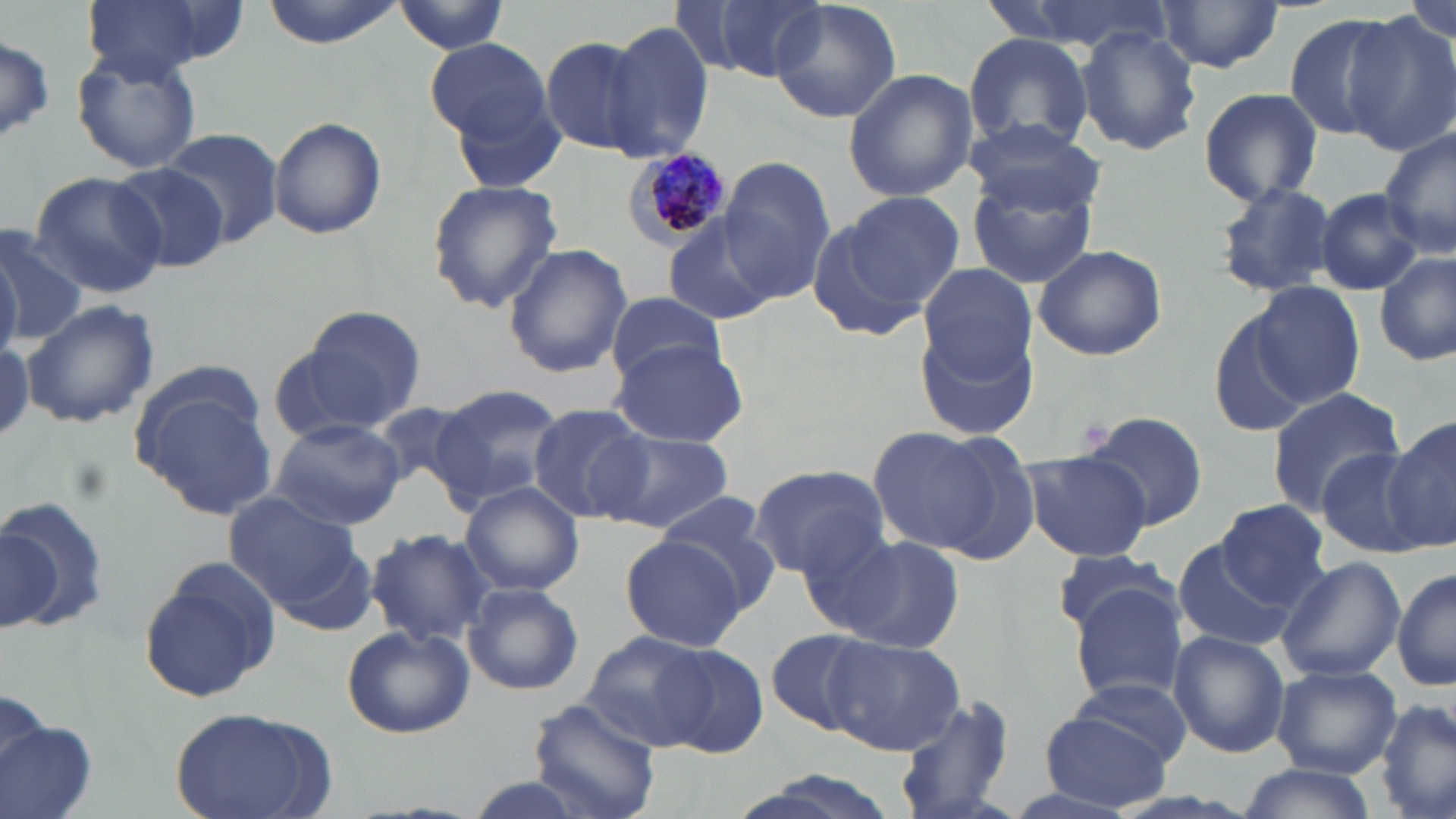

Summary:
  - Coordinate format: approximate bounding boxes as named x1/y1/x2/y2 corners in pixels
  - Plasmodium malariae-infected red blood cell locations: (x1=624, y1=147, x2=733, y2=248)
  - Uninfected red blood cell locations: (x1=76, y1=0, x2=222, y2=83), (x1=261, y1=0, x2=409, y2=49), (x1=394, y1=0, x2=511, y2=53), (x1=688, y1=0, x2=832, y2=82), (x1=768, y1=0, x2=902, y2=123), (x1=1406, y1=0, x2=1454, y2=45), (x1=1155, y1=2, x2=1284, y2=75), (x1=1282, y1=12, x2=1403, y2=141), (x1=1346, y1=12, x2=1456, y2=155), (x1=603, y1=20, x2=716, y2=161), (x1=1074, y1=22, x2=1202, y2=158), (x1=538, y1=33, x2=660, y2=158), (x1=961, y1=34, x2=1094, y2=154), (x1=0, y1=35, x2=55, y2=145), (x1=423, y1=36, x2=552, y2=141), (x1=71, y1=48, x2=202, y2=173), (x1=844, y1=68, x2=978, y2=202), (x1=1198, y1=86, x2=1323, y2=207), (x1=450, y1=91, x2=571, y2=192), (x1=268, y1=116, x2=386, y2=241), (x1=963, y1=118, x2=1103, y2=218), (x1=1378, y1=125, x2=1456, y2=259), (x1=158, y1=127, x2=284, y2=249), (x1=717, y1=157, x2=835, y2=302), (x1=107, y1=162, x2=231, y2=274), (x1=29, y1=171, x2=165, y2=297), (x1=965, y1=173, x2=1097, y2=290), (x1=425, y1=179, x2=563, y2=315), (x1=1211, y1=180, x2=1341, y2=300), (x1=1315, y1=188, x2=1426, y2=294), (x1=843, y1=192, x2=966, y2=311), (x1=663, y1=215, x2=772, y2=326), (x1=803, y1=215, x2=920, y2=342), (x1=0, y1=224, x2=86, y2=347), (x1=1032, y1=242, x2=1168, y2=361), (x1=502, y1=243, x2=632, y2=378), (x1=0, y1=244, x2=20, y2=364), (x1=1376, y1=250, x2=1454, y2=369), (x1=917, y1=262, x2=1037, y2=378), (x1=1249, y1=280, x2=1366, y2=406), (x1=605, y1=289, x2=725, y2=388), (x1=20, y1=300, x2=159, y2=431), (x1=1210, y1=304, x2=1318, y2=439), (x1=289, y1=305, x2=430, y2=434), (x1=916, y1=321, x2=1040, y2=444), (x1=608, y1=338, x2=754, y2=447), (x1=428, y1=384, x2=567, y2=510), (x1=1265, y1=387, x2=1408, y2=517), (x1=136, y1=389, x2=279, y2=520), (x1=528, y1=404, x2=655, y2=523), (x1=1078, y1=409, x2=1207, y2=534), (x1=1379, y1=415, x2=1456, y2=551), (x1=269, y1=418, x2=406, y2=530), (x1=869, y1=428, x2=1008, y2=554), (x1=597, y1=429, x2=734, y2=532), (x1=1318, y1=447, x2=1429, y2=557), (x1=1021, y1=450, x2=1155, y2=562), (x1=746, y1=465, x2=890, y2=577), (x1=460, y1=482, x2=584, y2=597), (x1=223, y1=491, x2=368, y2=622), (x1=657, y1=495, x2=777, y2=597), (x1=0, y1=498, x2=109, y2=637), (x1=1206, y1=502, x2=1331, y2=611), (x1=1, y1=524, x2=63, y2=632), (x1=791, y1=526, x2=911, y2=637), (x1=362, y1=528, x2=493, y2=648), (x1=828, y1=534, x2=964, y2=654), (x1=620, y1=536, x2=746, y2=651), (x1=1171, y1=537, x2=1296, y2=652), (x1=1049, y1=548, x2=1177, y2=635), (x1=1274, y1=556, x2=1405, y2=683), (x1=137, y1=558, x2=281, y2=703), (x1=1392, y1=568, x2=1456, y2=691), (x1=463, y1=583, x2=584, y2=696), (x1=1068, y1=585, x2=1191, y2=705), (x1=341, y1=624, x2=475, y2=740), (x1=581, y1=627, x2=718, y2=751), (x1=765, y1=627, x2=881, y2=738), (x1=1166, y1=629, x2=1289, y2=759), (x1=823, y1=634, x2=966, y2=755), (x1=655, y1=642, x2=768, y2=757), (x1=1271, y1=664, x2=1403, y2=779), (x1=1070, y1=674, x2=1193, y2=772), (x1=0, y1=690, x2=50, y2=786), (x1=893, y1=694, x2=1018, y2=819), (x1=1376, y1=696, x2=1455, y2=819), (x1=528, y1=698, x2=661, y2=819), (x1=167, y1=707, x2=337, y2=819), (x1=1038, y1=709, x2=1174, y2=811), (x1=2, y1=717, x2=93, y2=819), (x1=1236, y1=765, x2=1379, y2=819)
  - Slide-level diagnosis: Plasmodium malariae
  - Field of view: single
  - Preparation: thin blood film
  - Magnification: 1000x
  - Image size: 1456×819 pixels
  - Stain: May-Grünwald-Giemsa
  - Modality: optical microscopy